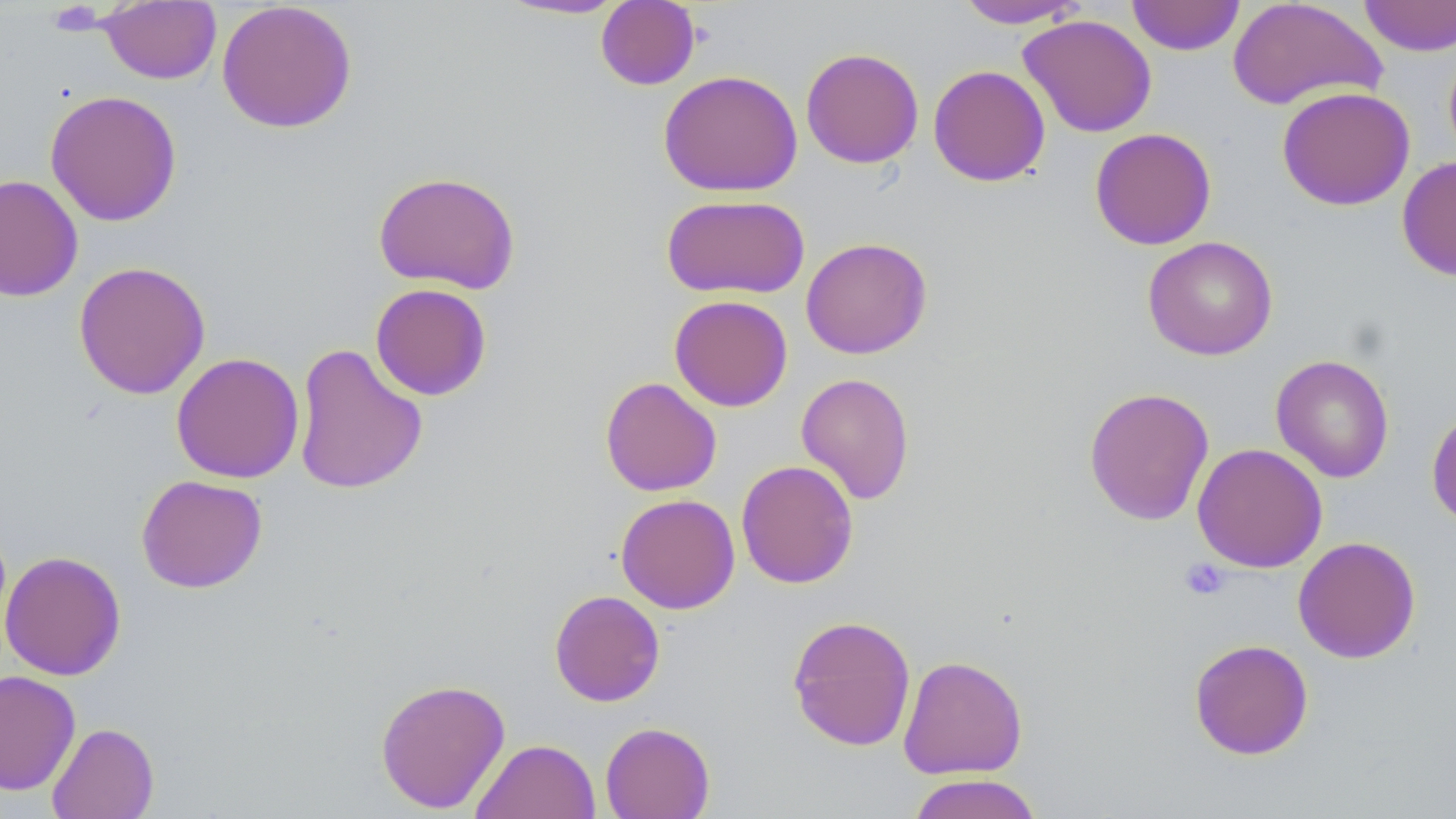

slide-level diagnosis = no evidence of blood parasites
image size = 1456×819 pixels
magnification = 1000x
platelet locations = approximate bounding boxes as named x1/y1/x2/y2 corners in pixels: (x1=1180, y1=558, x2=1231, y2=601)
preparation = thin blood smear
stain = May-Grünwald-Giemsa
field of view = single
modality = light microscopy
uninfected red blood cell locations = approximate bounding boxes as named x1/y1/x2/y2 corners in pixels: (x1=496, y1=0, x2=630, y2=21), (x1=955, y1=0, x2=1088, y2=29), (x1=1126, y1=0, x2=1245, y2=55), (x1=1226, y1=0, x2=1387, y2=112), (x1=1358, y1=0, x2=1456, y2=57), (x1=99, y1=1, x2=221, y2=85), (x1=216, y1=1, x2=358, y2=134), (x1=595, y1=1, x2=701, y2=90), (x1=1018, y1=14, x2=1157, y2=137), (x1=1443, y1=43, x2=1456, y2=166), (x1=800, y1=47, x2=924, y2=168), (x1=928, y1=64, x2=1051, y2=187), (x1=658, y1=69, x2=803, y2=197), (x1=1276, y1=86, x2=1415, y2=211), (x1=44, y1=89, x2=182, y2=227), (x1=1089, y1=127, x2=1217, y2=250), (x1=1396, y1=155, x2=1456, y2=282), (x1=372, y1=170, x2=521, y2=294), (x1=0, y1=174, x2=84, y2=302), (x1=660, y1=194, x2=810, y2=300), (x1=1142, y1=236, x2=1278, y2=360), (x1=800, y1=237, x2=932, y2=359), (x1=73, y1=260, x2=211, y2=400), (x1=370, y1=283, x2=492, y2=401), (x1=669, y1=295, x2=793, y2=411), (x1=292, y1=343, x2=428, y2=495), (x1=170, y1=352, x2=305, y2=483), (x1=1271, y1=354, x2=1395, y2=483), (x1=795, y1=373, x2=915, y2=505), (x1=599, y1=376, x2=722, y2=497), (x1=1083, y1=386, x2=1215, y2=526), (x1=1426, y1=405, x2=1456, y2=529), (x1=1192, y1=443, x2=1328, y2=573), (x1=735, y1=460, x2=858, y2=588), (x1=136, y1=474, x2=267, y2=593), (x1=615, y1=494, x2=740, y2=614), (x1=1292, y1=536, x2=1421, y2=663), (x1=0, y1=550, x2=126, y2=681), (x1=549, y1=589, x2=666, y2=707), (x1=787, y1=614, x2=916, y2=751), (x1=1188, y1=638, x2=1314, y2=760), (x1=898, y1=655, x2=1028, y2=779), (x1=0, y1=670, x2=81, y2=795), (x1=375, y1=677, x2=511, y2=814), (x1=600, y1=721, x2=715, y2=819), (x1=47, y1=722, x2=159, y2=819), (x1=470, y1=739, x2=601, y2=819), (x1=906, y1=773, x2=1044, y2=819)